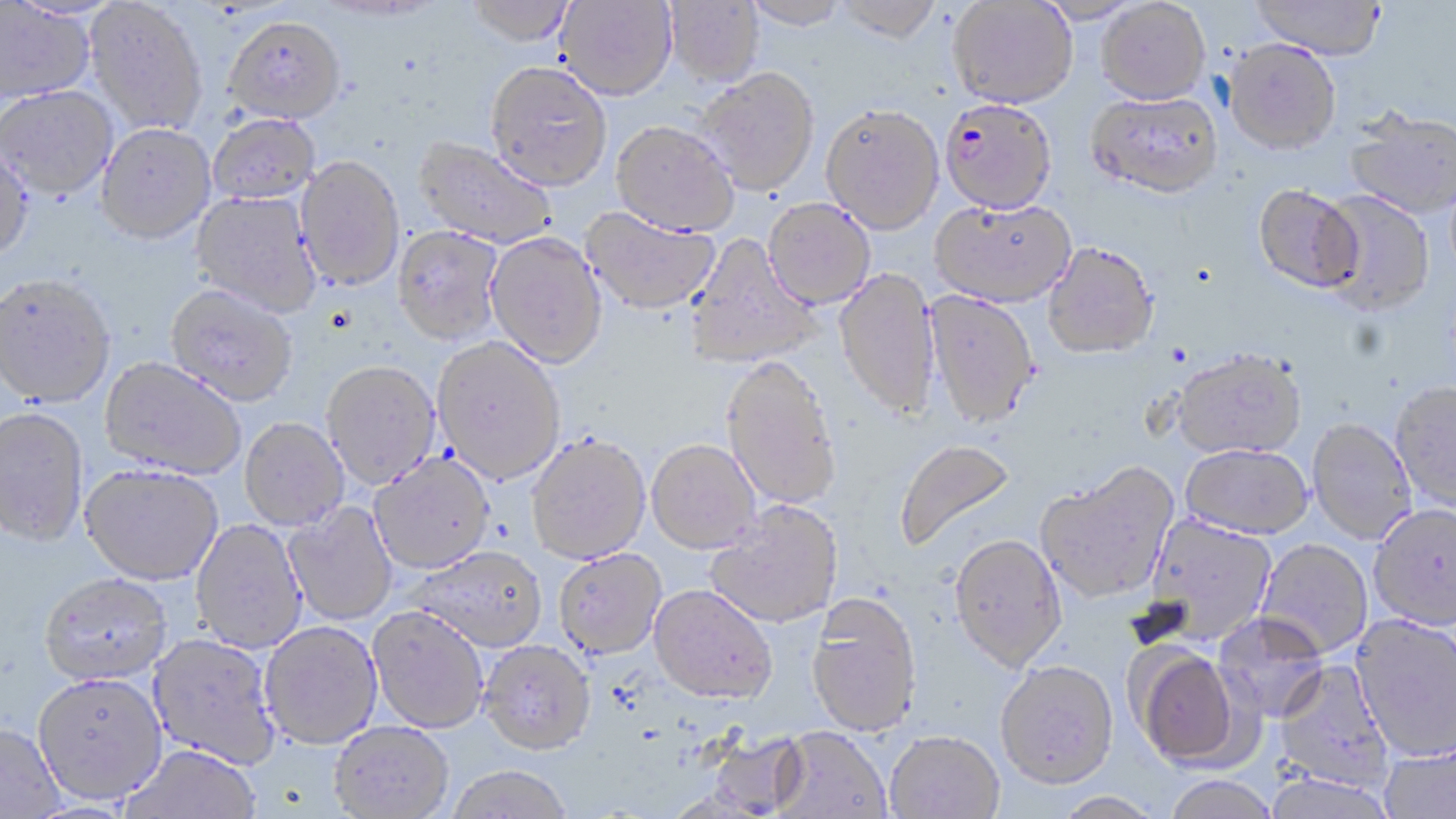

slide-level diagnosis = Plasmodium falciparum
field of view = one of a larger specimen
preparation = thin blood smear
modality = light microscopy
Plasmodium falciparum-infected red blood cell locations = approximate bounding boxes as (x1, y1, x2, y2) in pixels: (939, 97, 1057, 214)
uninfected red blood cell locations = approximate bounding boxes as (x1, y1, x2, y2) in pixels: (462, 0, 577, 47), (554, 0, 678, 102), (742, 0, 851, 29), (833, 0, 944, 43), (1250, 0, 1386, 58), (84, 1, 208, 137), (664, 1, 764, 87), (948, 1, 1078, 108), (1096, 1, 1211, 104), (0, 2, 96, 105), (224, 17, 346, 125), (1223, 38, 1341, 154), (485, 63, 612, 192), (696, 68, 821, 197), (0, 86, 119, 203), (1087, 91, 1223, 197), (821, 103, 944, 234), (1344, 109, 1456, 218), (208, 114, 321, 207), (611, 121, 739, 237), (95, 125, 216, 247), (412, 137, 557, 250), (0, 145, 35, 265), (294, 158, 405, 293), (1252, 183, 1363, 293), (1318, 189, 1434, 315), (189, 191, 321, 318), (763, 198, 876, 310), (930, 198, 1076, 306), (581, 208, 720, 316), (392, 228, 504, 348), (485, 233, 608, 370), (685, 234, 821, 370), (1043, 241, 1158, 359), (834, 269, 940, 420), (0, 276, 116, 410), (164, 286, 297, 409), (924, 290, 1040, 430), (432, 339, 565, 486), (1172, 348, 1307, 459), (721, 357, 841, 511), (99, 359, 246, 481), (321, 364, 441, 492), (1390, 382, 1456, 512), (0, 409, 90, 550), (1307, 418, 1416, 543), (239, 419, 349, 531), (526, 435, 651, 566), (894, 440, 1018, 553), (646, 441, 760, 555), (1181, 444, 1313, 539), (369, 456, 496, 576), (1036, 463, 1178, 604), (80, 466, 223, 588), (706, 501, 842, 629), (283, 502, 398, 626), (1368, 503, 1456, 631), (1141, 514, 1277, 646), (190, 519, 308, 655), (949, 534, 1068, 672), (1256, 539, 1372, 658), (411, 549, 547, 654), (554, 549, 667, 661), (39, 576, 171, 689), (649, 586, 778, 707), (806, 593, 923, 737), (367, 608, 488, 735), (1212, 612, 1330, 723), (1351, 614, 1456, 762), (260, 623, 383, 751), (147, 635, 281, 771), (479, 641, 596, 758), (1132, 647, 1246, 769), (1273, 659, 1393, 791), (995, 660, 1119, 789), (33, 677, 167, 808), (330, 723, 454, 818), (0, 726, 65, 818), (771, 727, 890, 819), (703, 729, 809, 817), (884, 731, 1004, 819), (1380, 740, 1456, 819), (119, 747, 261, 819), (445, 768, 573, 819), (1163, 776, 1278, 819), (1052, 792, 1165, 819)
image size = 1456×819 pixels
magnification = 1000x
stain = May-Grünwald-Giemsa